Classify this cell by malaria status.
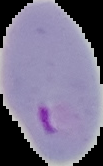
Parasitized.

From a thin blood film. The area outside the segmented cell region is set to black. Image is 103×166 pixels.